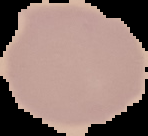
Summary:
  - Image type: cell region segmented out of the field of view; surrounding area masked to black
  - Preparation: thin blood film
  - Malaria status: uninfected
  - Image size: 148×136 pixels